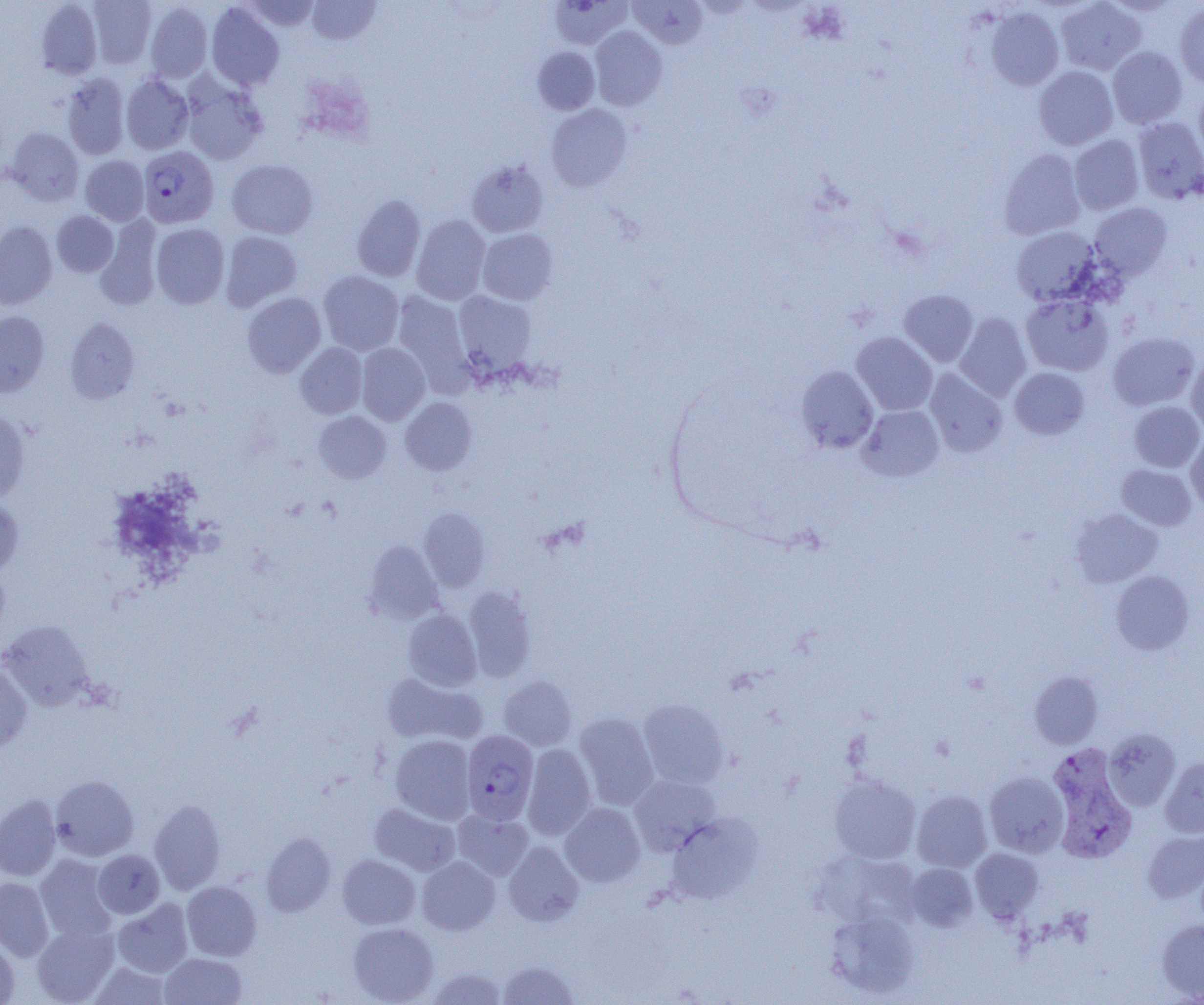
{
  "slide_level_diagnosis": "Plasmodium vivax",
  "modality": "light microscopy",
  "field_of_view": "one of a larger specimen",
  "magnification": "1000x",
  "uninfected_red_blood_cell_locations": "approximate bounding boxes as named x1/y1/x2/y2 corners in pixels: (x1=88, y1=0, x2=156, y2=68), (x1=307, y1=0, x2=381, y2=45), (x1=628, y1=0, x2=708, y2=49), (x1=1055, y1=0, x2=1146, y2=75), (x1=36, y1=1, x2=102, y2=79), (x1=241, y1=1, x2=322, y2=31), (x1=549, y1=1, x2=632, y2=49), (x1=144, y1=2, x2=213, y2=82), (x1=206, y1=3, x2=284, y2=91), (x1=1175, y1=3, x2=1204, y2=88), (x1=985, y1=6, x2=1064, y2=91), (x1=589, y1=25, x2=668, y2=111), (x1=533, y1=46, x2=600, y2=114), (x1=1107, y1=47, x2=1187, y2=129), (x1=1033, y1=66, x2=1118, y2=150), (x1=61, y1=73, x2=130, y2=159), (x1=121, y1=74, x2=193, y2=155), (x1=180, y1=76, x2=268, y2=165), (x1=1193, y1=86, x2=1204, y2=167), (x1=546, y1=104, x2=632, y2=191), (x1=1132, y1=117, x2=1204, y2=204), (x1=6, y1=128, x2=83, y2=205), (x1=1069, y1=134, x2=1144, y2=214), (x1=999, y1=148, x2=1086, y2=239), (x1=80, y1=156, x2=149, y2=225), (x1=226, y1=159, x2=318, y2=239), (x1=466, y1=159, x2=549, y2=238), (x1=352, y1=194, x2=426, y2=282), (x1=1089, y1=202, x2=1172, y2=280), (x1=52, y1=211, x2=118, y2=276), (x1=411, y1=215, x2=490, y2=305), (x1=96, y1=216, x2=162, y2=310), (x1=0, y1=222, x2=57, y2=309), (x1=151, y1=223, x2=230, y2=308), (x1=1011, y1=226, x2=1101, y2=306), (x1=477, y1=228, x2=558, y2=305), (x1=220, y1=231, x2=302, y2=311), (x1=318, y1=270, x2=404, y2=356), (x1=899, y1=289, x2=978, y2=366), (x1=391, y1=291, x2=472, y2=391), (x1=454, y1=291, x2=537, y2=372), (x1=242, y1=292, x2=326, y2=378), (x1=1020, y1=293, x2=1113, y2=376), (x1=0, y1=311, x2=49, y2=397), (x1=954, y1=313, x2=1032, y2=401), (x1=65, y1=317, x2=139, y2=404), (x1=1108, y1=331, x2=1199, y2=410), (x1=851, y1=332, x2=938, y2=416), (x1=295, y1=342, x2=367, y2=418), (x1=356, y1=343, x2=430, y2=425), (x1=1186, y1=356, x2=1204, y2=433), (x1=795, y1=365, x2=879, y2=453), (x1=1009, y1=367, x2=1089, y2=440), (x1=924, y1=369, x2=1007, y2=457), (x1=400, y1=397, x2=477, y2=475), (x1=1129, y1=401, x2=1204, y2=472), (x1=858, y1=405, x2=944, y2=482), (x1=0, y1=409, x2=31, y2=503), (x1=313, y1=411, x2=391, y2=483), (x1=1186, y1=433, x2=1204, y2=510), (x1=1116, y1=464, x2=1196, y2=530), (x1=0, y1=497, x2=23, y2=575), (x1=418, y1=508, x2=490, y2=592), (x1=1070, y1=509, x2=1163, y2=587), (x1=364, y1=540, x2=443, y2=623), (x1=1110, y1=571, x2=1195, y2=655), (x1=462, y1=585, x2=537, y2=681), (x1=402, y1=608, x2=482, y2=691), (x1=0, y1=621, x2=95, y2=712), (x1=0, y1=663, x2=33, y2=753), (x1=1030, y1=671, x2=1103, y2=749), (x1=381, y1=672, x2=487, y2=747), (x1=498, y1=675, x2=576, y2=751), (x1=638, y1=699, x2=728, y2=789), (x1=573, y1=712, x2=659, y2=810), (x1=1104, y1=728, x2=1181, y2=810), (x1=390, y1=734, x2=476, y2=823), (x1=522, y1=744, x2=596, y2=840), (x1=1160, y1=757, x2=1204, y2=838), (x1=984, y1=772, x2=1069, y2=857), (x1=829, y1=773, x2=921, y2=863), (x1=629, y1=774, x2=720, y2=855), (x1=50, y1=775, x2=139, y2=861), (x1=912, y1=790, x2=992, y2=872), (x1=0, y1=795, x2=62, y2=881), (x1=149, y1=799, x2=226, y2=894), (x1=560, y1=802, x2=645, y2=887), (x1=369, y1=803, x2=460, y2=876), (x1=453, y1=809, x2=534, y2=880), (x1=664, y1=812, x2=761, y2=904), (x1=1143, y1=830, x2=1204, y2=903), (x1=261, y1=832, x2=336, y2=917), (x1=504, y1=841, x2=584, y2=926), (x1=970, y1=848, x2=1043, y2=923), (x1=92, y1=849, x2=165, y2=919), (x1=337, y1=854, x2=420, y2=929), (x1=34, y1=855, x2=118, y2=942), (x1=417, y1=856, x2=500, y2=935), (x1=906, y1=863, x2=978, y2=931), (x1=0, y1=877, x2=54, y2=961), (x1=182, y1=881, x2=261, y2=961), (x1=112, y1=898, x2=193, y2=977), (x1=827, y1=907, x2=919, y2=998), (x1=1157, y1=918, x2=1204, y2=999), (x1=31, y1=922, x2=119, y2=1004), (x1=348, y1=922, x2=439, y2=1004), (x1=0, y1=936, x2=19, y2=1004), (x1=160, y1=952, x2=247, y2=1005), (x1=498, y1=959, x2=578, y2=1004), (x1=89, y1=961, x2=171, y2=1004), (x1=426, y1=966, x2=507, y2=1004)",
  "preparation": "thin blood film",
  "plasmodium_vivax_infected_red_blood_cell_locations": "approximate bounding boxes as named x1/y1/x2/y2 corners in pixels: (x1=137, y1=146, x2=219, y2=228), (x1=462, y1=729, x2=539, y2=825), (x1=1043, y1=744, x2=1135, y2=866)",
  "image_size": "1204×1005 pixels"
}